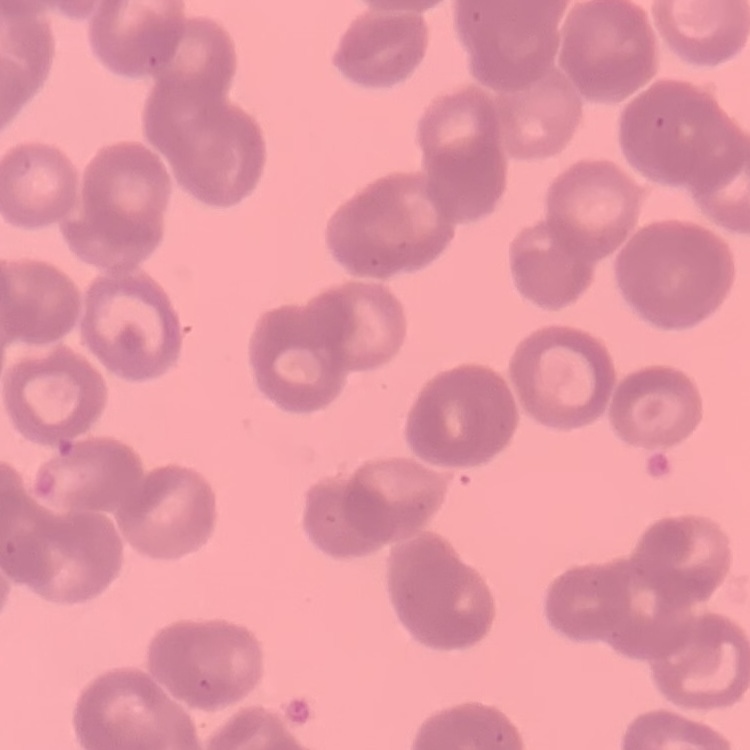

The red blood cells exhibit rouleaux formation. Field's or Giemsa stain. Thin peripheral smear. One tile cut from a larger photomicrograph.